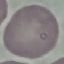 Result: no malaria parasites seen. Thin blood smear. Automatically extracted cell patch, resized to 64 × 64 pixels. Acquired by smartphone through the microscope eyepiece. Giemsa stain.